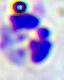

A white blood cell is shown. Photomicrograph. Captured at 400x magnification.